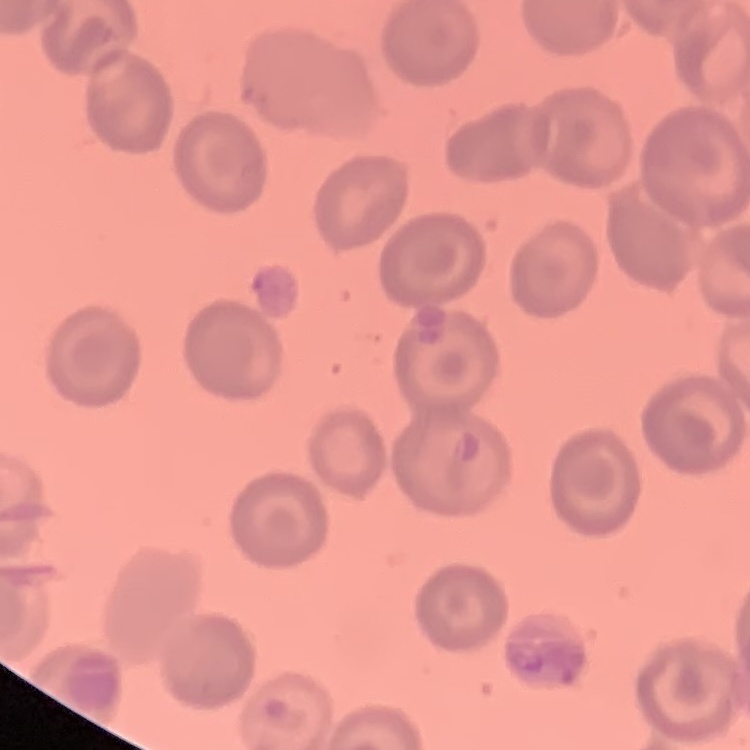

The erythrocytes show no rouleaux formation. Square crop of a larger photomicrograph. Thin blood film. Stained with either Field's or Giemsa.